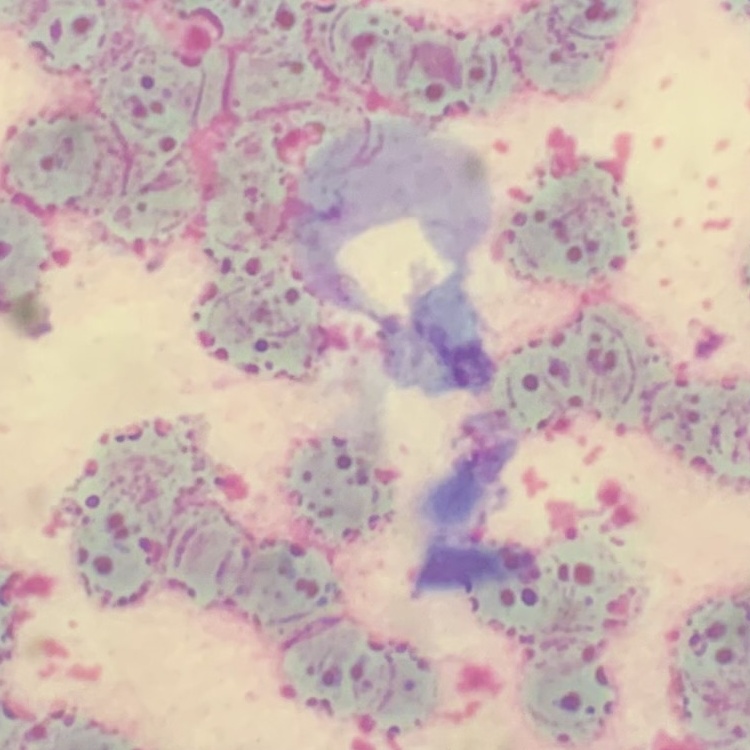 The red blood cells exhibit rouleaux formation. Thin blood smear. Square crop of a larger photomicrograph. Stained with either Field's or Giemsa.